Identify the cell.
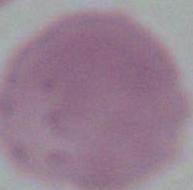
This is an erythrocyte.

1000x magnification. Photomicrograph.